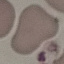

{
  "result": "no malaria parasites detected",
  "image_type": "cell patch, automatically extracted from a larger field of view and resized to 64 × 64 pixels",
  "capture": "smartphone through the microscope eyepiece",
  "preparation": "thin blood film",
  "stain": "Giemsa"
}